Assess this cell for malaria.
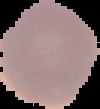

Uninfected.

Summary:
  - Image type: segmented cell region on a black background
  - Image size: 100×109 pixels
  - Preparation: thin blood smear